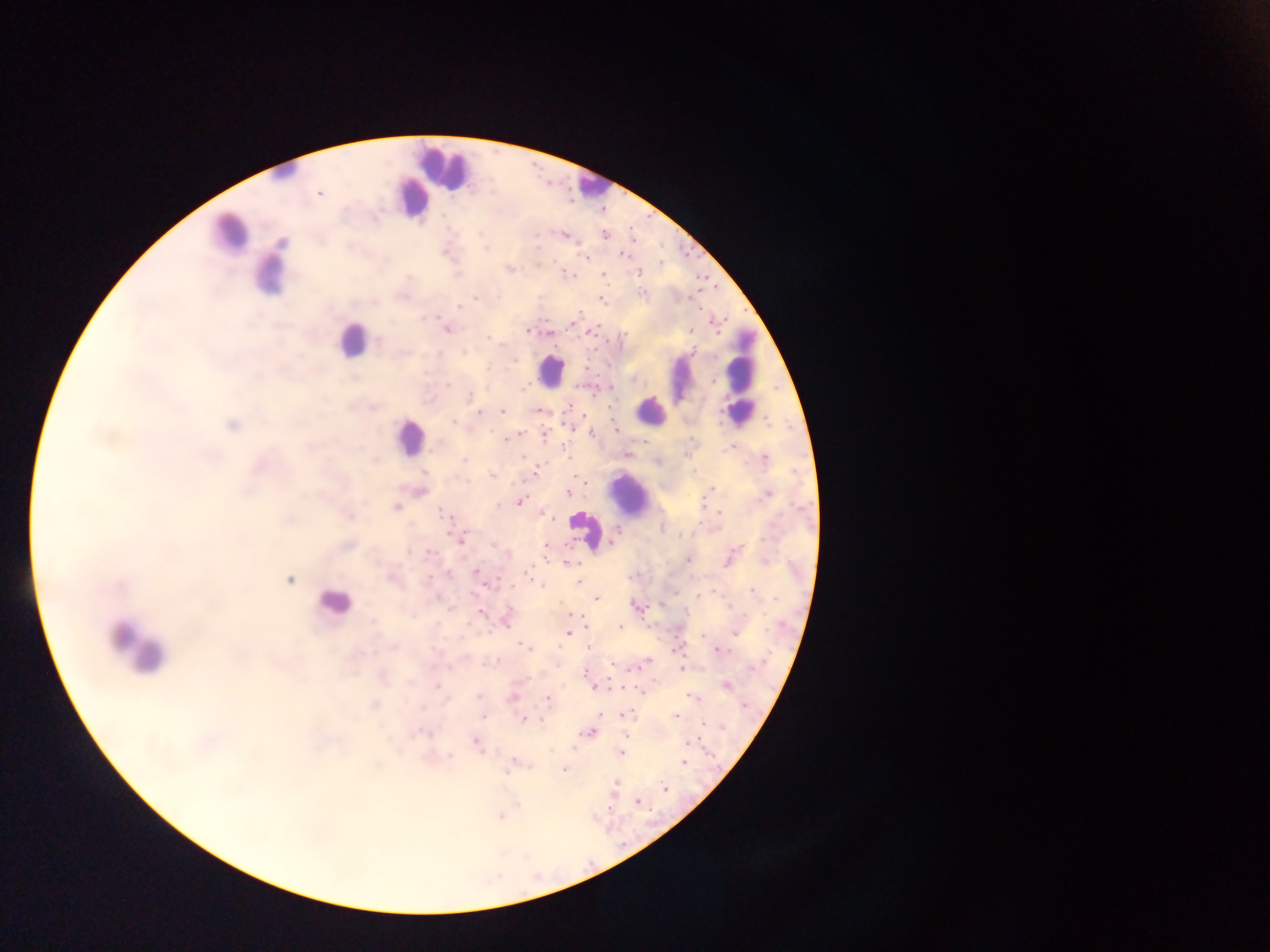

{
  "country": "Ghana",
  "leukocyte_locations": "approximate centers as {x, y} in pixels: {443, 165}, {282, 176}, {592, 183}, {411, 193}, {226, 238}, {268, 278}, {355, 341}, {739, 345}, {553, 371}, {680, 380}, {650, 407}, {410, 441}, {634, 500}, {586, 530}, {330, 603}, {136, 655}",
  "preparation": "thick blood film",
  "field_of_view": "single",
  "capture": "mobile-phone photograph through a microscope",
  "malaria_parasite_locations": "approximate centers as {x, y} in pixels: {321, 193}, {415, 216}, {376, 217}, {563, 235}, {605, 236}, {569, 237}, {535, 238}, {282, 242}, {349, 246}, {487, 249}, {586, 256}, {624, 256}, {536, 261}, {507, 267}, {564, 272}, {567, 273}, {639, 273}, {408, 276}, {605, 276}, {275, 292}, {643, 294}, {476, 297}, {600, 299}, {373, 301}, {458, 305}, {698, 306}, {426, 317}, {433, 317}, {577, 318}, {446, 329}, {527, 329}, {594, 331}, {548, 332}, {487, 337}, {380, 340}, {512, 361}, {448, 384}, {469, 398}, {179, 407}, {370, 407}, {502, 410}, {479, 411}, {539, 411}, {767, 421}, {454, 422}, {231, 425}, {615, 429}, {590, 432}, {93, 435}, {544, 435}, {115, 438}, {503, 438}, {729, 442}, {566, 453}, {209, 456}, {765, 458}, {464, 459}, {536, 468}, {532, 474}, {490, 475}, {580, 478}, {584, 480}, {711, 488}, {244, 490}, {568, 493}, {768, 494}, {703, 501}, {519, 502}, {395, 506}, {718, 511}, {157, 513}, {443, 513}, {545, 514}, {97, 515}, {349, 516}, {288, 518}, {616, 533}, {463, 539}, {493, 546}, {174, 550}, {409, 552}, {728, 560}, {765, 560}, {568, 562}, {476, 569}, {391, 578}, {288, 580}, {427, 581}, {579, 581}, {121, 585}, {752, 590}, {474, 594}, {596, 598}, {632, 604}, {448, 607}, {570, 613}, {481, 615}, {372, 623}, {504, 624}, {586, 628}, {621, 628}, {735, 632}, {566, 633}, {394, 647}, {523, 647}, {719, 650}, {239, 657}, {270, 658}, {277, 660}, {493, 662}, {648, 662}, {615, 665}, {352, 669}, {682, 670}, {586, 675}, {384, 676}, {589, 685}, {436, 686}, {726, 686}, {641, 692}, {478, 695}, {692, 698}, {547, 700}, {374, 705}, {625, 714}, {480, 717}, {675, 717}, {524, 720}, {701, 724}, {589, 732}, {429, 734}, {622, 734}, {473, 741}, {687, 742}, {571, 748}, {316, 749}, {622, 754}, {255, 755}, {448, 757}, {682, 763}, {378, 766}, {563, 770}, {616, 782}, {663, 788}, {233, 789}, {661, 789}, {636, 802}, {500, 818}",
  "image_size": "1270×952 pixels"
}